Locate the cells, classifying each as a parasitized RBC, an uninfected RBC, or a WBC.
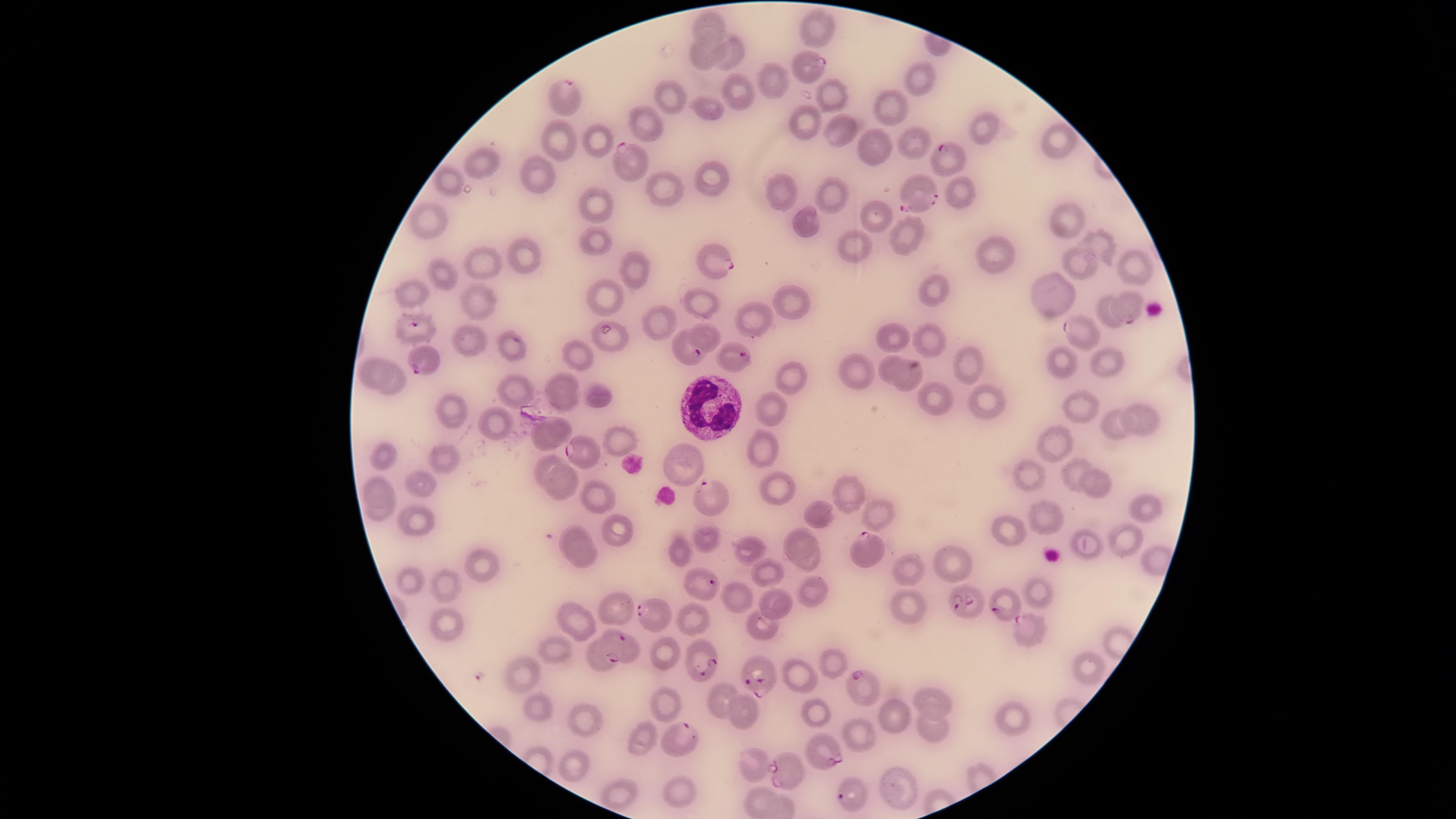

Approximate marker points as [x, y] in pixels.
Parasitized RBCs: [809, 64], [566, 98], [938, 162], [626, 164], [922, 190], [714, 257], [1127, 307], [412, 328], [1076, 334], [689, 351], [733, 358], [423, 359], [580, 453], [709, 497], [862, 549], [701, 586], [1002, 604], [967, 605], [653, 616], [1025, 627], [612, 644], [702, 660], [756, 669], [861, 684], [680, 738], [822, 747], [785, 768], [850, 798].
Uninfected RBCs: [711, 30], [821, 31], [703, 50], [733, 57], [773, 80], [919, 82], [737, 96], [831, 96], [669, 97], [707, 105], [890, 108], [647, 123], [806, 123], [987, 128], [841, 131], [557, 139], [598, 141], [872, 141], [913, 141], [1057, 141], [484, 163], [538, 175], [709, 175], [446, 183], [777, 187], [954, 191], [668, 192], [833, 196], [596, 204], [1070, 217], [881, 220], [425, 222], [804, 225], [909, 236], [591, 244], [1101, 246], [851, 248], [520, 254], [993, 254], [484, 262], [1084, 264], [1134, 267], [630, 271], [443, 275], [936, 289], [1051, 291], [410, 293], [608, 295], [476, 301], [697, 302], [785, 305], [1105, 311], [754, 318], [660, 319], [471, 338], [927, 339], [890, 340], [610, 341], [509, 347], [579, 353], [1109, 362], [962, 363], [889, 364], [1063, 366], [374, 372], [791, 374], [912, 376], [560, 380], [399, 381], [857, 382], [518, 391], [600, 395], [928, 400], [988, 400], [565, 404], [1078, 409], [453, 410], [768, 412], [1145, 417], [1114, 425], [498, 427], [551, 435], [618, 436], [1054, 439], [759, 448], [443, 458], [385, 461], [546, 464], [684, 466], [1072, 470], [1028, 475], [560, 478], [1095, 483], [423, 485], [376, 488], [776, 490], [845, 493], [600, 498], [1146, 508], [877, 511], [374, 513], [824, 515], [1045, 516], [420, 519], [1009, 532], [614, 534], [577, 537], [704, 537], [796, 539], [1125, 541], [749, 548], [1090, 549], [677, 550], [583, 560], [948, 560], [805, 562], [482, 568], [763, 568], [905, 573], [415, 581], [446, 588], [1039, 589], [811, 594], [740, 598], [773, 600], [904, 605], [612, 611], [695, 618], [574, 622], [449, 624], [763, 628], [559, 650], [633, 654], [663, 654], [600, 659], [1084, 666], [833, 667], [522, 673], [794, 677], [719, 697], [927, 700], [663, 702], [535, 708], [815, 711], [893, 714], [1008, 716], [587, 717], [748, 717], [927, 727], [863, 736], [649, 740], [755, 764], [572, 765], [899, 788], [678, 791], [620, 792], [761, 802].
WBCs: [709, 407].

Circular visible region. Giemsa-stained preparation. Species: Plasmodium falciparum. Image is 1456×819 pixels. Photographed with a smartphone camera through the microscope eyepiece. Thin blood smear. One field of view of the specimen.